Locate and identify every blood parasite.
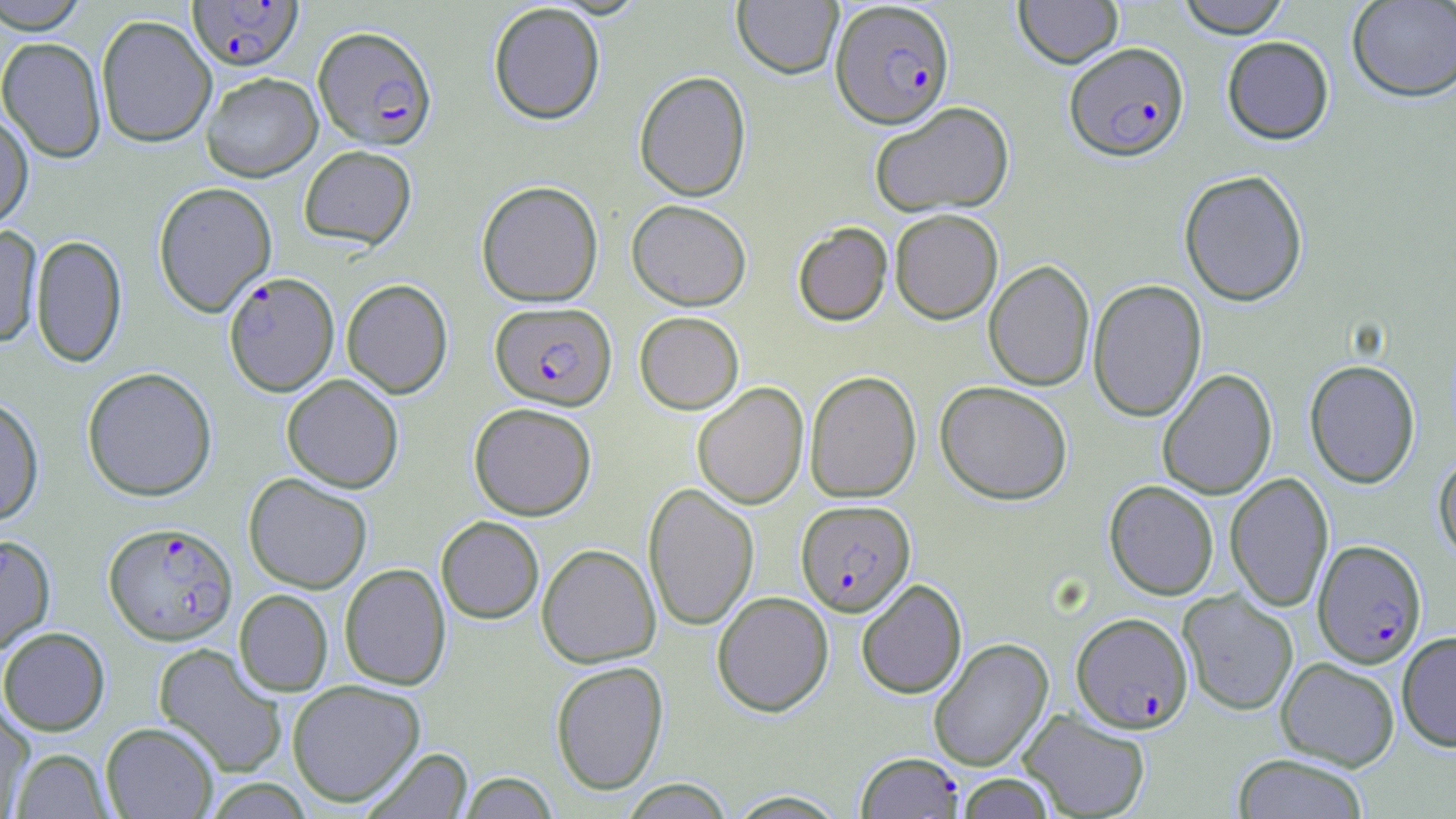

Approximate bounding boxes as (x1,y1)-(x2,y2) corner pairs in pixels.
Plasmodium falciparum-infected red blood cells: (188,1)-(303,71), (829,1)-(955,128), (313,25)-(437,151), (1065,42)-(1189,161), (223,270)-(339,395), (490,301)-(617,410), (796,499)-(915,617), (104,522)-(237,644), (1312,539)-(1426,668), (1072,612)-(1193,732), (855,752)-(964,818).
No Plasmodium ovale, Plasmodium malariae, Plasmodium vivax, Babesia divergens, or Trypanosoma brucei observed.

Summary:
  - Uninfected red blood cell locations: (732,0)-(843,79), (1014,0)-(1123,67), (1176,0)-(1292,37), (1346,0)-(1456,101), (0,1)-(92,33), (488,3)-(605,124), (96,14)-(217,148), (1222,36)-(1334,143), (0,37)-(107,162), (634,70)-(752,201), (201,72)-(322,181), (869,101)-(1014,217), (0,111)-(34,231), (298,145)-(417,249), (1179,169)-(1308,306), (476,180)-(603,307), (153,181)-(276,317), (626,199)-(751,311), (890,209)-(1003,324), (792,222)-(893,326), (0,223)-(43,348), (31,234)-(127,367), (984,260)-(1095,391), (341,279)-(453,398), (1087,279)-(1206,422), (634,311)-(744,414), (1304,359)-(1420,488), (81,367)-(217,501), (1157,369)-(1277,499), (804,370)-(921,503), (281,374)-(404,492), (935,381)-(1073,504), (692,382)-(808,509), (0,396)-(44,525), (469,402)-(597,520), (1433,452)-(1456,563), (1225,472)-(1333,612), (243,473)-(372,593), (1104,480)-(1219,600), (643,482)-(759,632), (436,516)-(544,623), (0,533)-(56,655), (537,543)-(660,668), (340,563)-(451,690), (856,579)-(967,699), (234,589)-(333,696), (1179,590)-(1298,716), (712,591)-(834,716), (0,627)-(110,735), (1397,630)-(1456,752), (928,637)-(1053,771), (152,642)-(287,778), (1276,657)-(1400,771), (550,660)-(669,795), (287,679)-(426,807), (0,702)-(34,817), (1018,708)-(1151,818), (100,722)-(219,818), (11,748)-(113,818), (362,748)-(472,818), (1232,753)-(1370,819), (457,772)-(559,818), (955,773)-(1057,818), (618,779)-(735,818), (725,790)-(850,818)
  - Slide-level diagnosis: Plasmodium falciparum
  - Preparation: thin blood film
  - Magnification: 1000x
  - Modality: light microscopy
  - Image size: 1456×819 pixels
  - Field of view: single
  - Stain: May-Grünwald-Giemsa